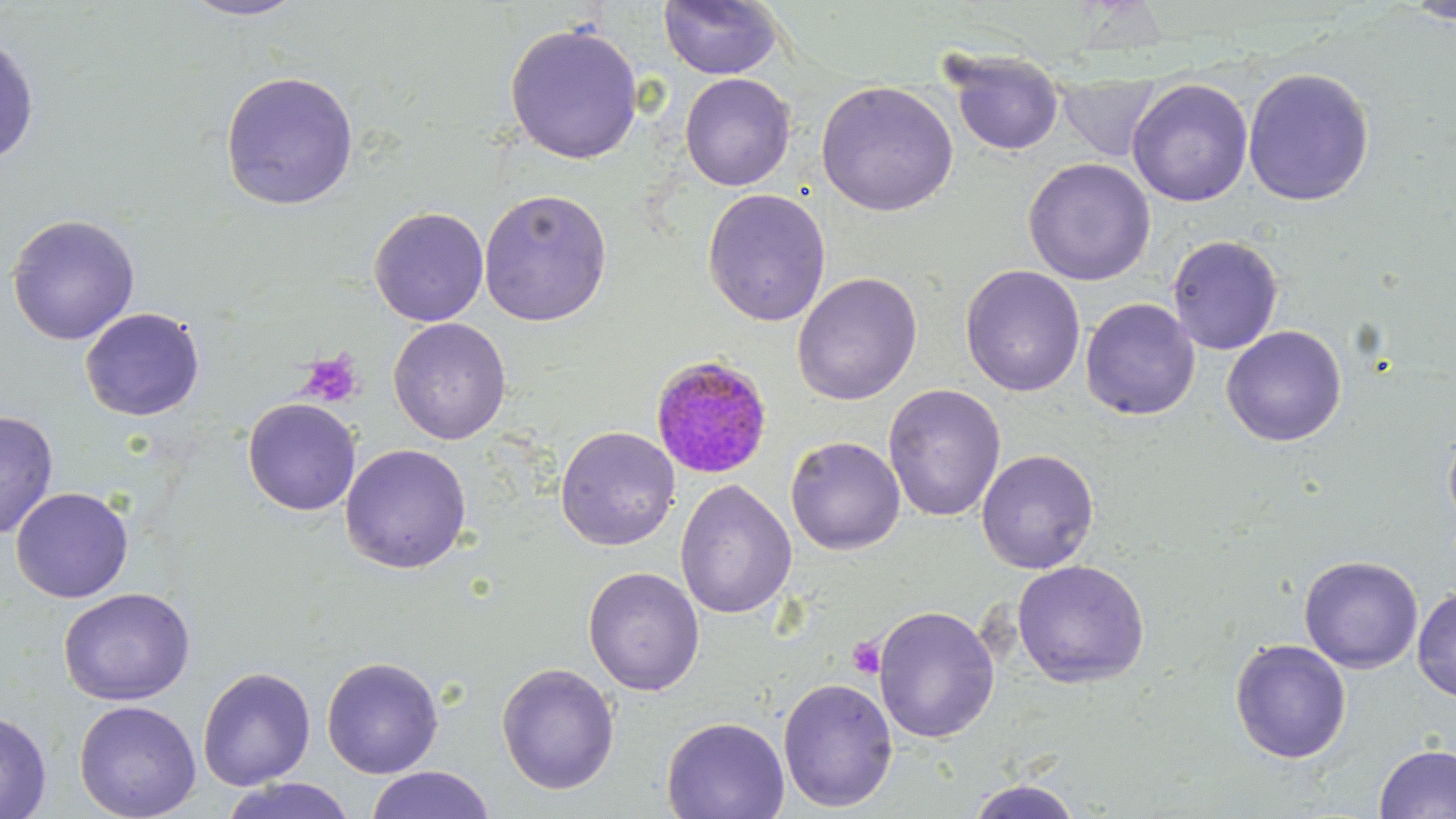

slide_level_diagnosis: Plasmodium malariae
field_of_view: one of a larger specimen
image_size: 1456×819 pixels
platelet_locations: 'approximate bounding boxes as named x1/y1/x2/y2 corners in pixels: (x1=297, y1=351, x2=364, y2=408), (x1=847, y1=637, x2=887, y2=679)'
modality: optical microscopy
stain: May-Grünwald-Giemsa
magnification: 1000x
preparation: thin blood film
plasmodium_malariae_infected_red_blood_cell_locations: 'approximate bounding boxes as named x1/y1/x2/y2 corners in pixels: (x1=651, y1=354, x2=774, y2=478)'
uninfected_red_blood_cell_locations: 'approximate bounding boxes as named x1/y1/x2/y2 corners in pixels: (x1=179, y1=0, x2=307, y2=21), (x1=658, y1=0, x2=784, y2=80), (x1=1401, y1=0, x2=1456, y2=24), (x1=504, y1=22, x2=644, y2=166), (x1=0, y1=31, x2=40, y2=165), (x1=944, y1=49, x2=1065, y2=157), (x1=1242, y1=67, x2=1375, y2=206), (x1=219, y1=70, x2=359, y2=211), (x1=679, y1=72, x2=796, y2=192), (x1=1057, y1=75, x2=1162, y2=163), (x1=1126, y1=78, x2=1254, y2=207), (x1=816, y1=80, x2=959, y2=217), (x1=1023, y1=157, x2=1156, y2=286), (x1=477, y1=188, x2=614, y2=327), (x1=702, y1=188, x2=832, y2=327), (x1=369, y1=206, x2=489, y2=326), (x1=6, y1=213, x2=141, y2=346), (x1=1167, y1=234, x2=1284, y2=356), (x1=959, y1=264, x2=1086, y2=397), (x1=791, y1=271, x2=923, y2=406), (x1=1080, y1=297, x2=1200, y2=420), (x1=80, y1=308, x2=205, y2=421), (x1=388, y1=317, x2=512, y2=445), (x1=1221, y1=325, x2=1347, y2=447), (x1=883, y1=383, x2=1006, y2=522), (x1=242, y1=398, x2=361, y2=516), (x1=0, y1=410, x2=60, y2=540), (x1=1442, y1=421, x2=1456, y2=533), (x1=555, y1=425, x2=680, y2=551), (x1=785, y1=436, x2=906, y2=555), (x1=339, y1=443, x2=472, y2=574), (x1=976, y1=448, x2=1100, y2=574), (x1=674, y1=479, x2=797, y2=620), (x1=10, y1=487, x2=133, y2=603), (x1=1298, y1=554, x2=1423, y2=673), (x1=1012, y1=559, x2=1150, y2=688), (x1=582, y1=566, x2=705, y2=695), (x1=58, y1=588, x2=196, y2=706), (x1=1412, y1=589, x2=1456, y2=702), (x1=873, y1=605, x2=1000, y2=743), (x1=1229, y1=638, x2=1352, y2=764), (x1=321, y1=656, x2=444, y2=779), (x1=496, y1=662, x2=620, y2=795), (x1=197, y1=666, x2=316, y2=790), (x1=777, y1=677, x2=899, y2=812), (x1=74, y1=699, x2=202, y2=819), (x1=0, y1=710, x2=52, y2=819), (x1=661, y1=715, x2=790, y2=819), (x1=1374, y1=743, x2=1456, y2=819), (x1=365, y1=766, x2=495, y2=819), (x1=219, y1=777, x2=357, y2=819), (x1=965, y1=778, x2=1082, y2=819)'